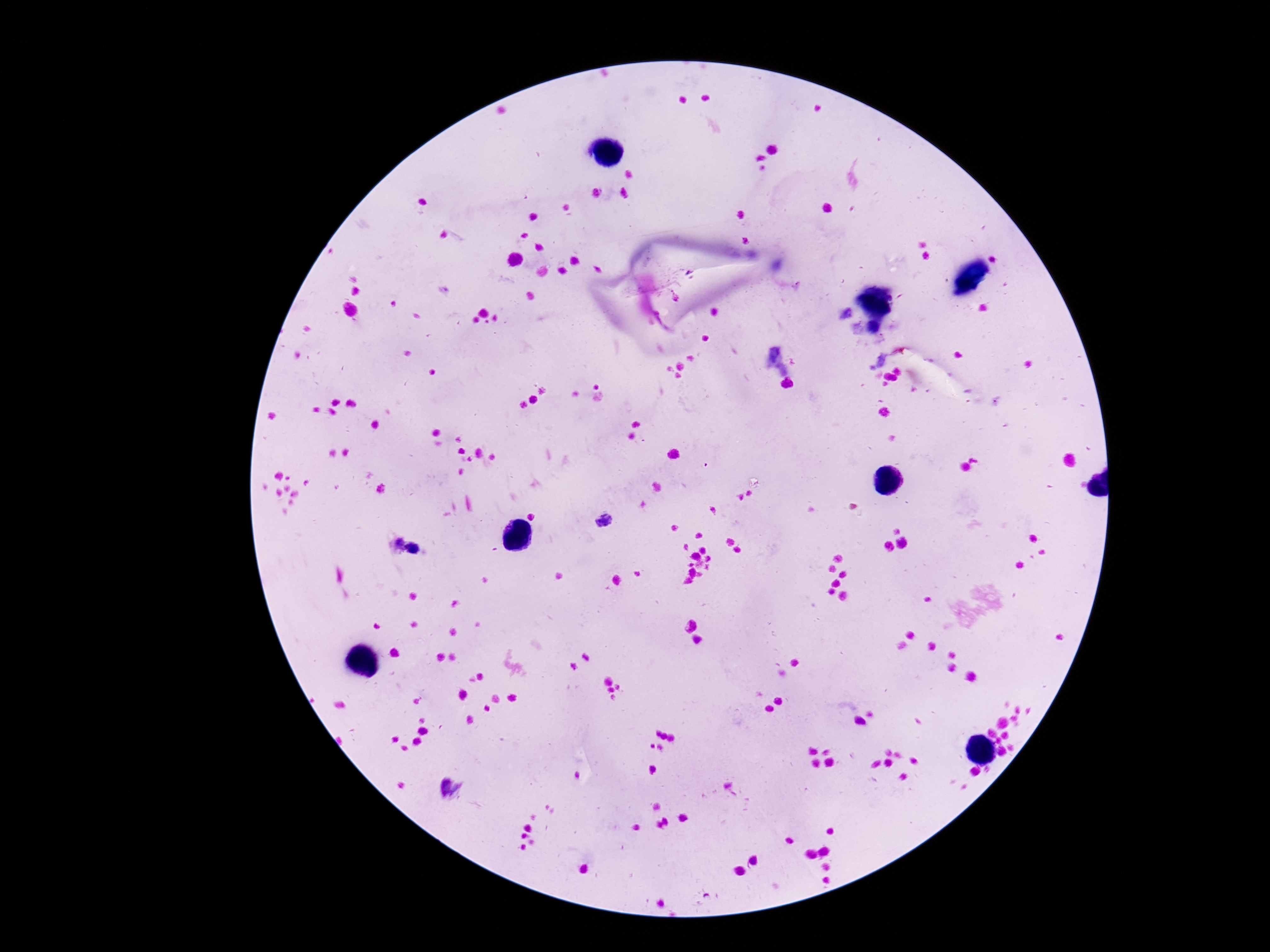

Approximate centers as (x, y) in pixels. Plasmodium parasite locations: (604, 522), (398, 544), (412, 549). Photographed through the microscope eyepiece with a smartphone camera. Image is 1270×952 pixels. Thick blood smear. Patient malaria status: positive. 100x magnification. Giemsa-stained preparation. Single field of view.